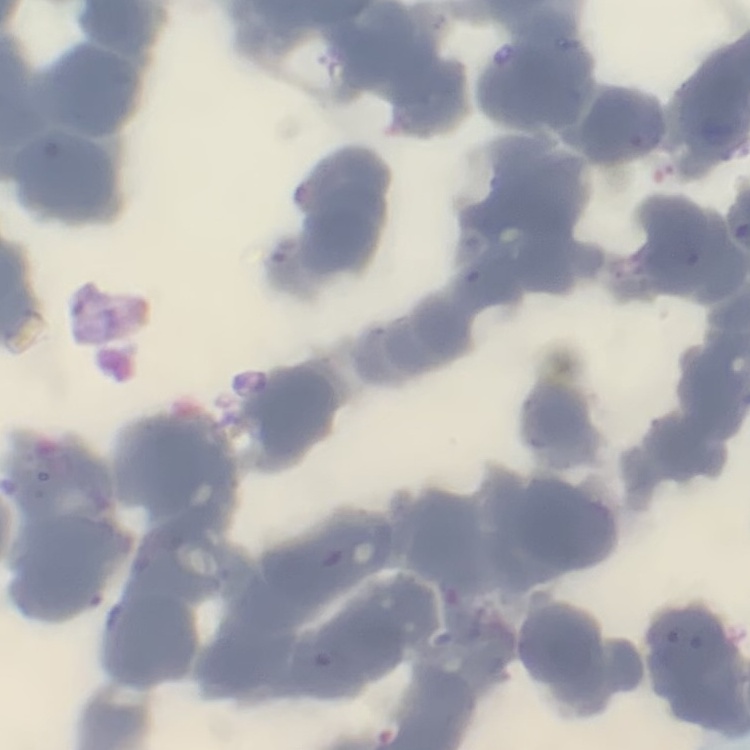

red blood cell morphology = rouleaux formation
image type = square crop of a larger photomicrograph
preparation = thin blood smear
stain = Field's or Giemsa